Comment on the morphology of the erythrocytes.
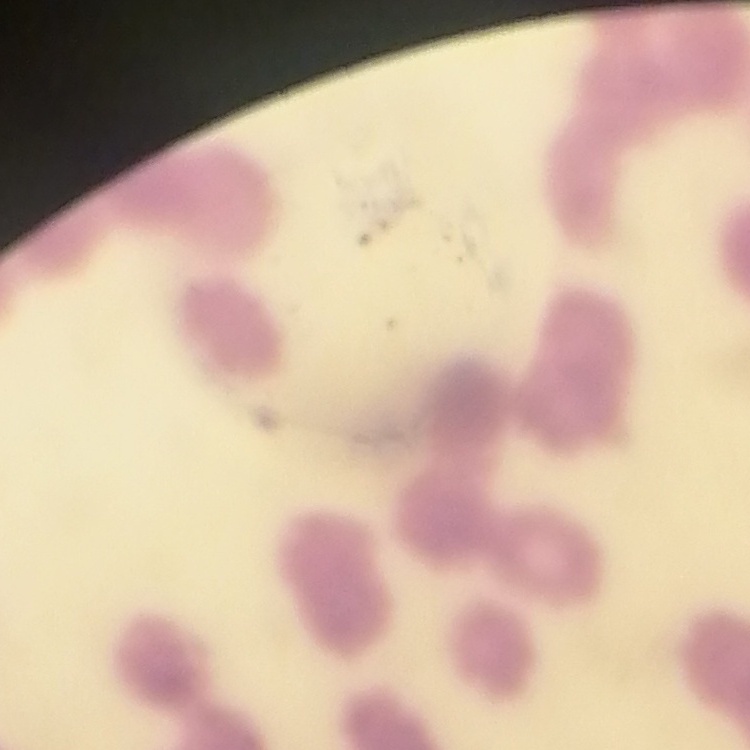

They show rouleaux formation.

Summary:
  - Preparation: thin blood smear
  - Image type: one tile cut from a larger photomicrograph
  - Stain: Field's or Giemsa